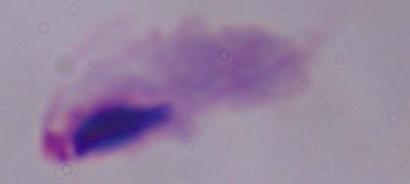
identification = trichomonad
magnification = 1000x
modality = micrograph